Classify this cell by malaria status.
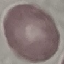

Uninfected.

preparation = thin smear
image type = cell patch, automatically extracted from a larger field of view and resized to 64 × 64 pixels
capture = smartphone through the microscope eyepiece
stain = Giemsa